State which parasite is depicted.
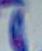
This is Toxoplasma gondii.

magnification = 1000x
modality = micrograph